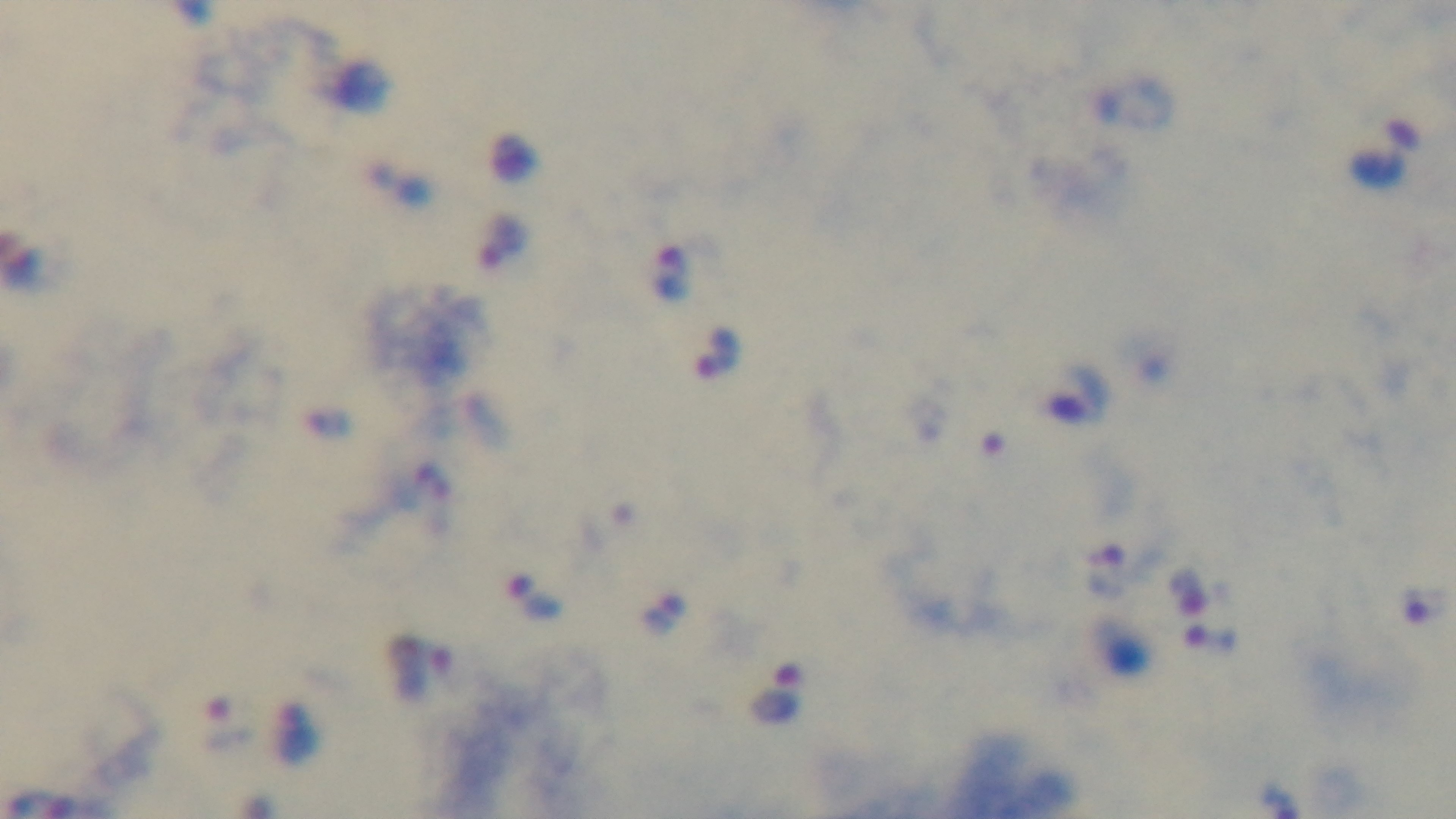 Giemsa-stained. Preparation: thick blood film. Malaria status: infected. Oil-immersion objective, 100x. Captured with a mounted 4K digital camera. Photomicrograph. Single field of view.